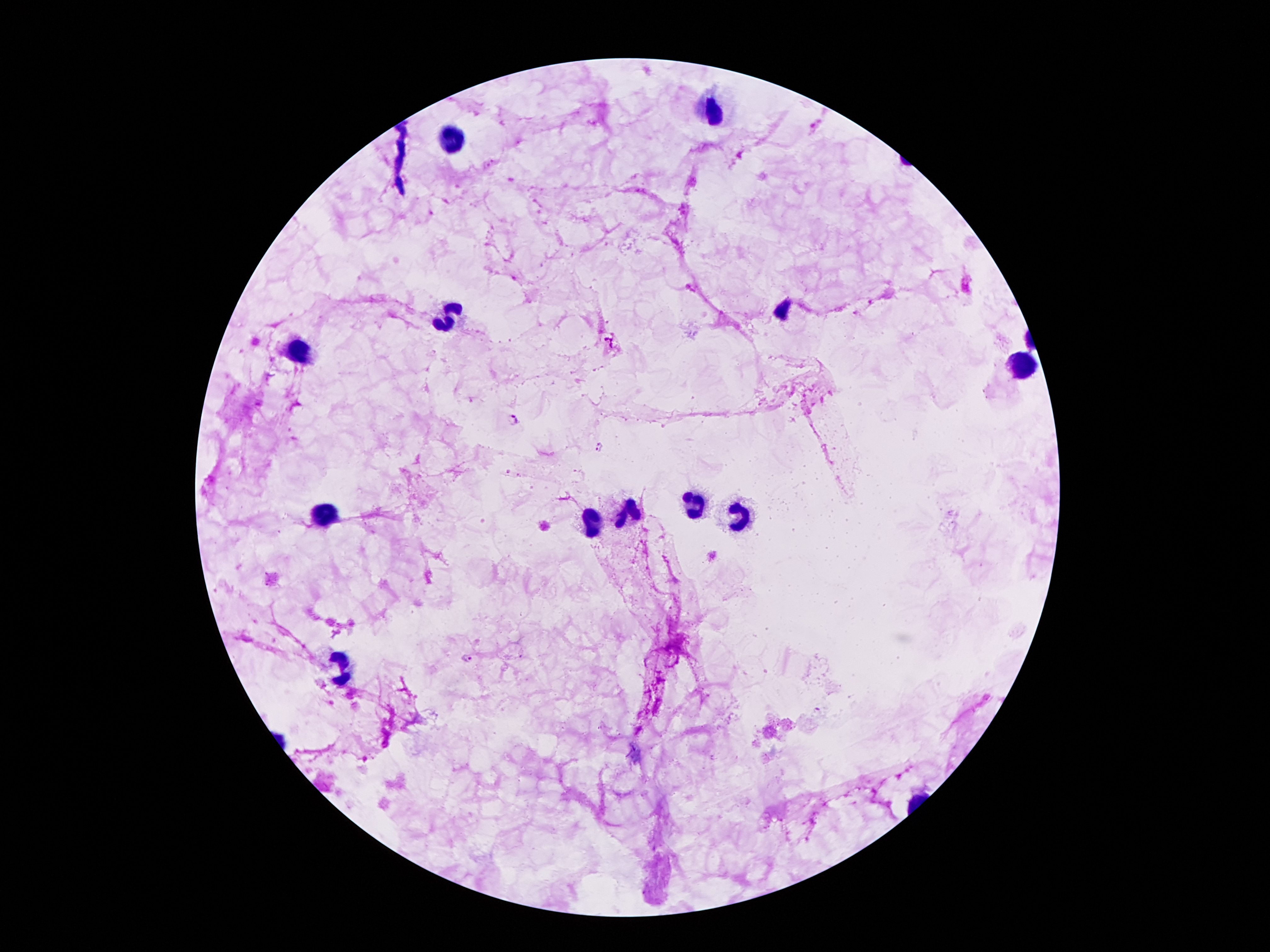
coordinate format = approximate centers as (x, y) in pixels
leukocyte locations = (717, 112), (449, 145), (451, 319), (299, 351), (1022, 365), (697, 505), (630, 510), (330, 514), (739, 516), (588, 522), (345, 671)
Plasmodium parasite locations = (515, 420), (599, 447), (467, 657)
preparation = thick blood smear
stain = Giemsa
field of view = single
magnification = 100x
image size = 1270×952 pixels
patient malaria status = infected with Plasmodium falciparum
capture = smartphone camera through the microscope eyepiece